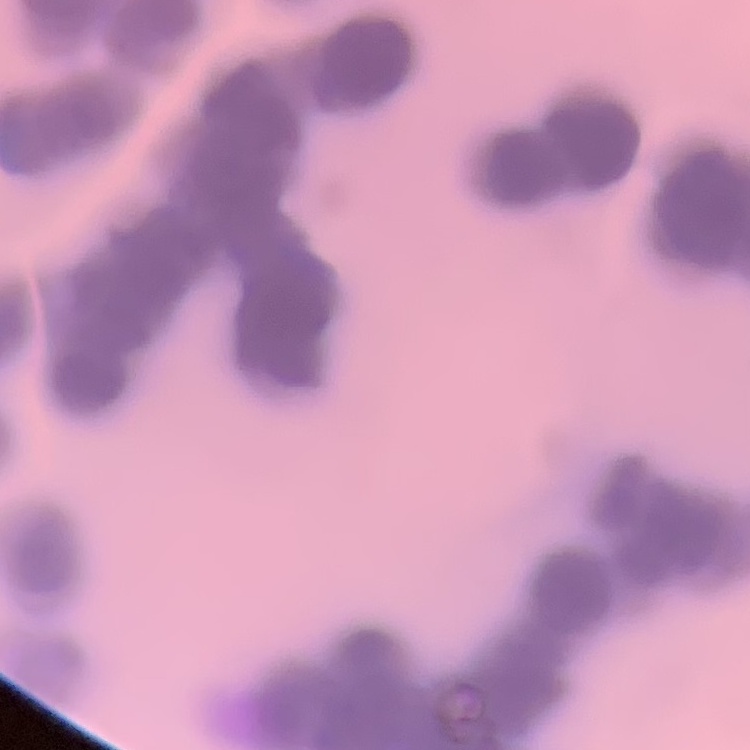

The red blood cells exhibit rouleaux formation. Stained with either Field's or Giemsa. Square crop of a larger photomicrograph. Thin peripheral smear.